Name the cell type shown.
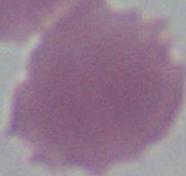
This is an erythrocyte.

Photomicrograph. Captured at 1000x magnification.